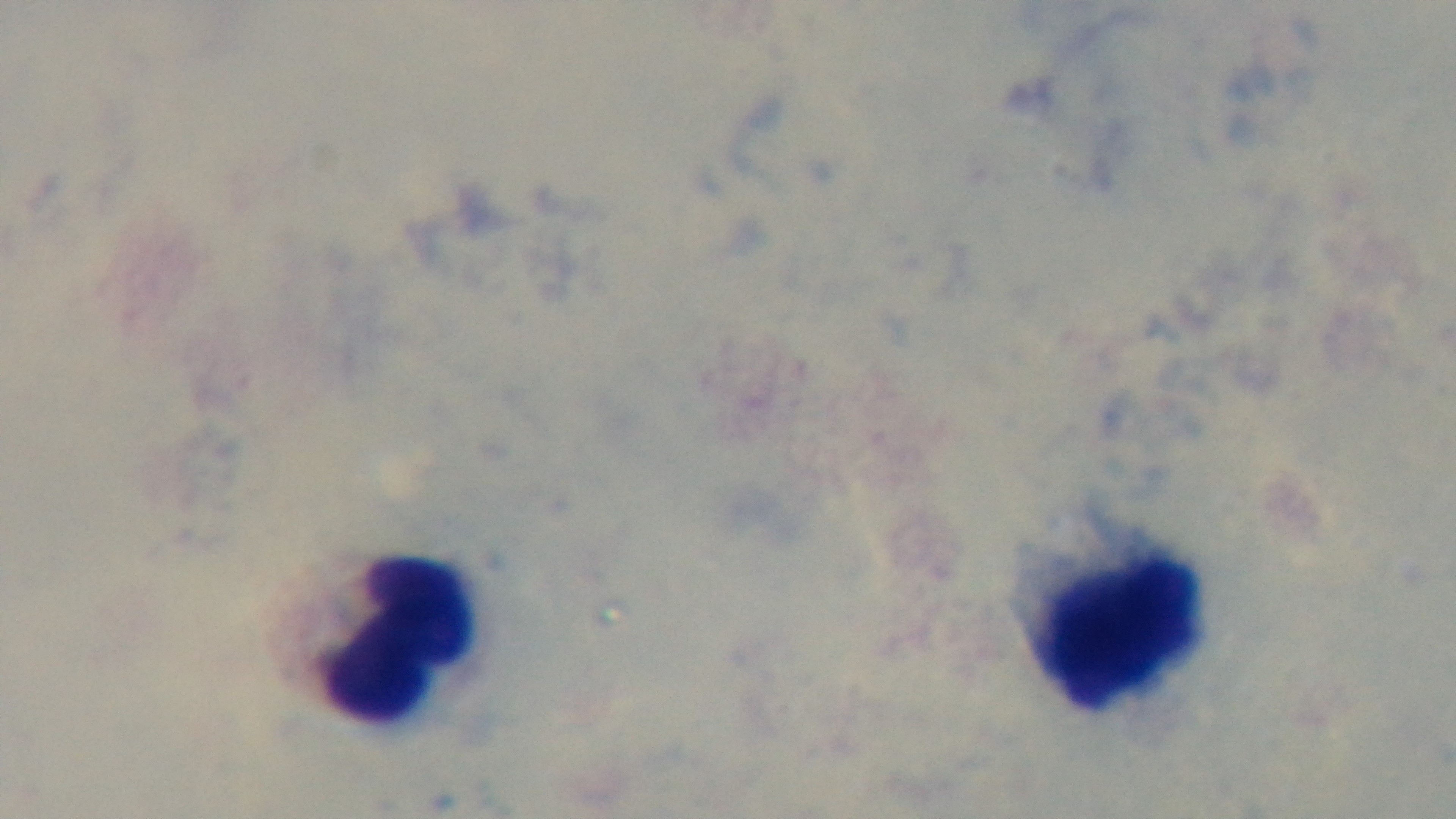
{
  "field_of_view": "single",
  "preparation": "thick",
  "capture": "mounted 4K digital camera",
  "objective": "100x oil immersion",
  "malaria_status": "negative",
  "stain": "Giemsa",
  "modality": "light microscopy"
}